Identify the cell.
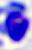
A leukocyte.

Summary:
  - Modality: photomicrograph
  - Magnification: 400x